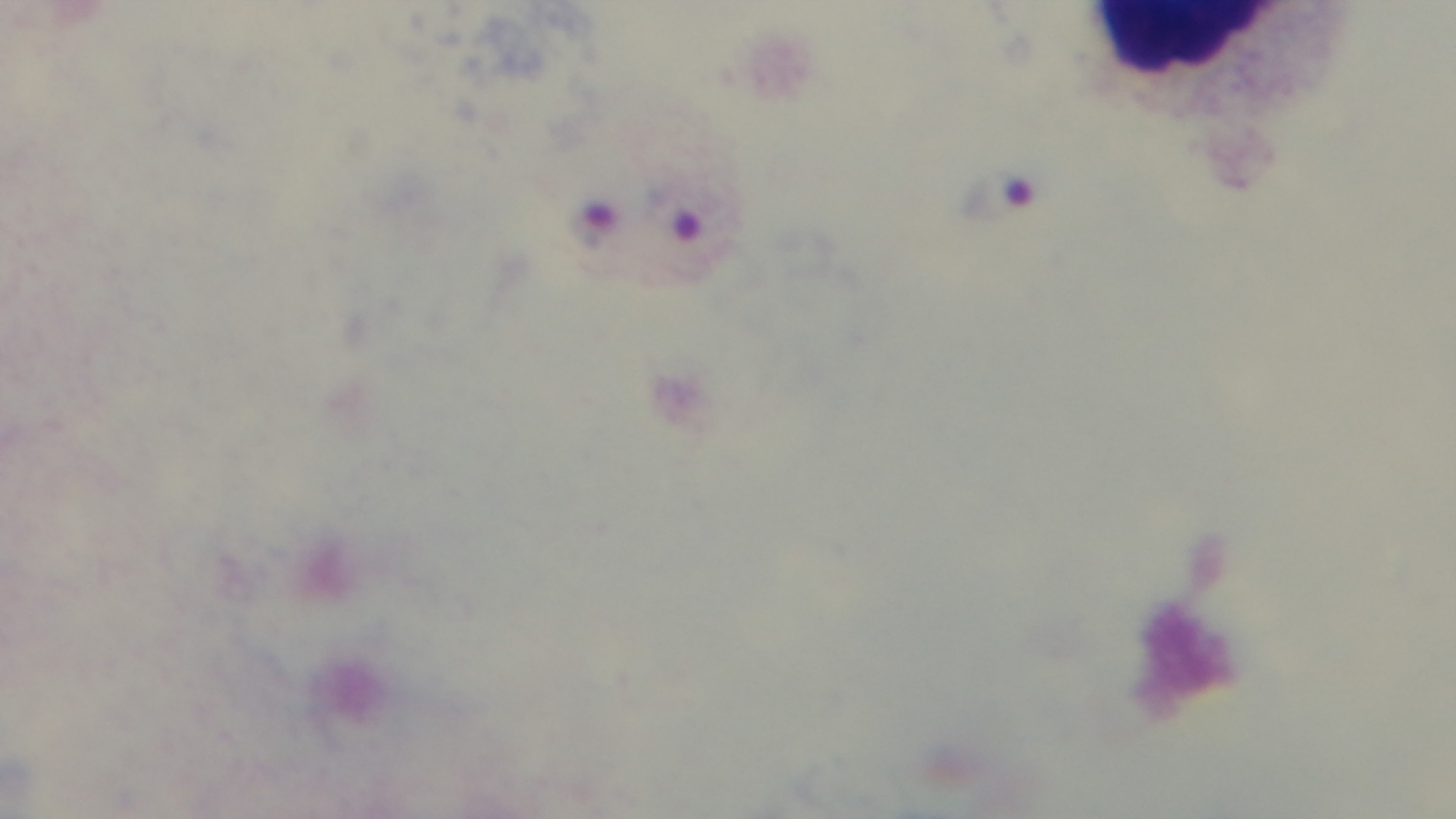
Summary:
  - Stain: Giemsa
  - Malaria status: infected
  - Field of view: single
  - Objective: 100x oil immersion
  - Capture: mounted 4K digital camera
  - Preparation: thick blood film
  - Modality: light microscopy